Assess this cell for malaria.
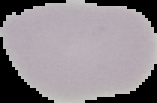

It is uninfected.

From a thin blood film. Image is 157×103 pixels. Segmented cell region on a black background.